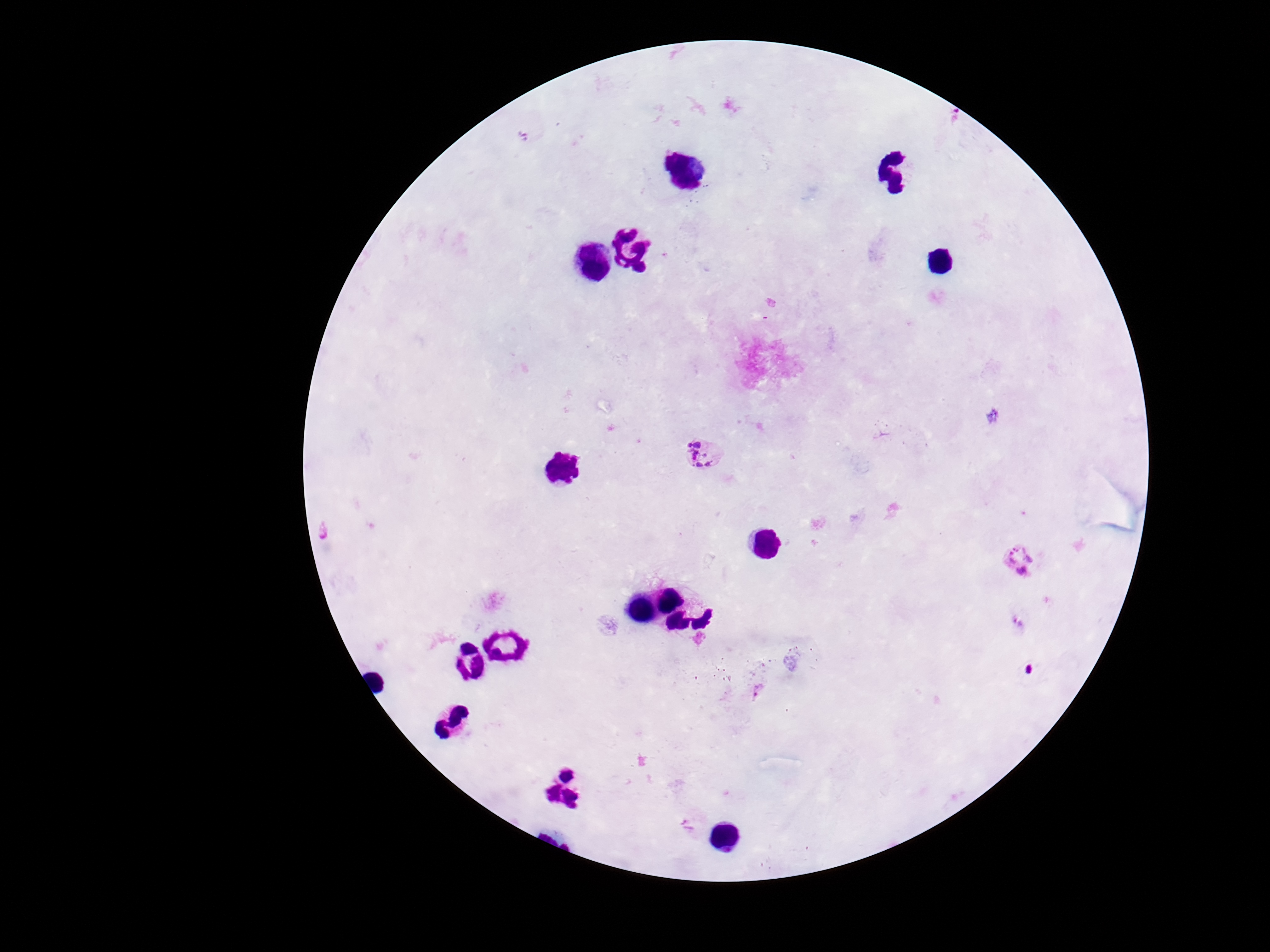

{
  "field_of_view": "one from this slide",
  "patient_malaria_status": "positive",
  "preparation": "thick blood smear",
  "stain": "Giemsa",
  "image_size": "1270×952 pixels",
  "plasmodium_parasite_locations": "approximate centers as (x, y) in pixels: (702, 455), (1020, 560), (758, 689), (689, 823)",
  "capture": "smartphone camera through the microscope eyepiece",
  "magnification": "100x"
}